State which parasite is depicted.
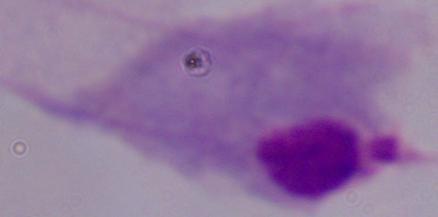

A trichomonad.

modality = photomicrograph
magnification = 1000x